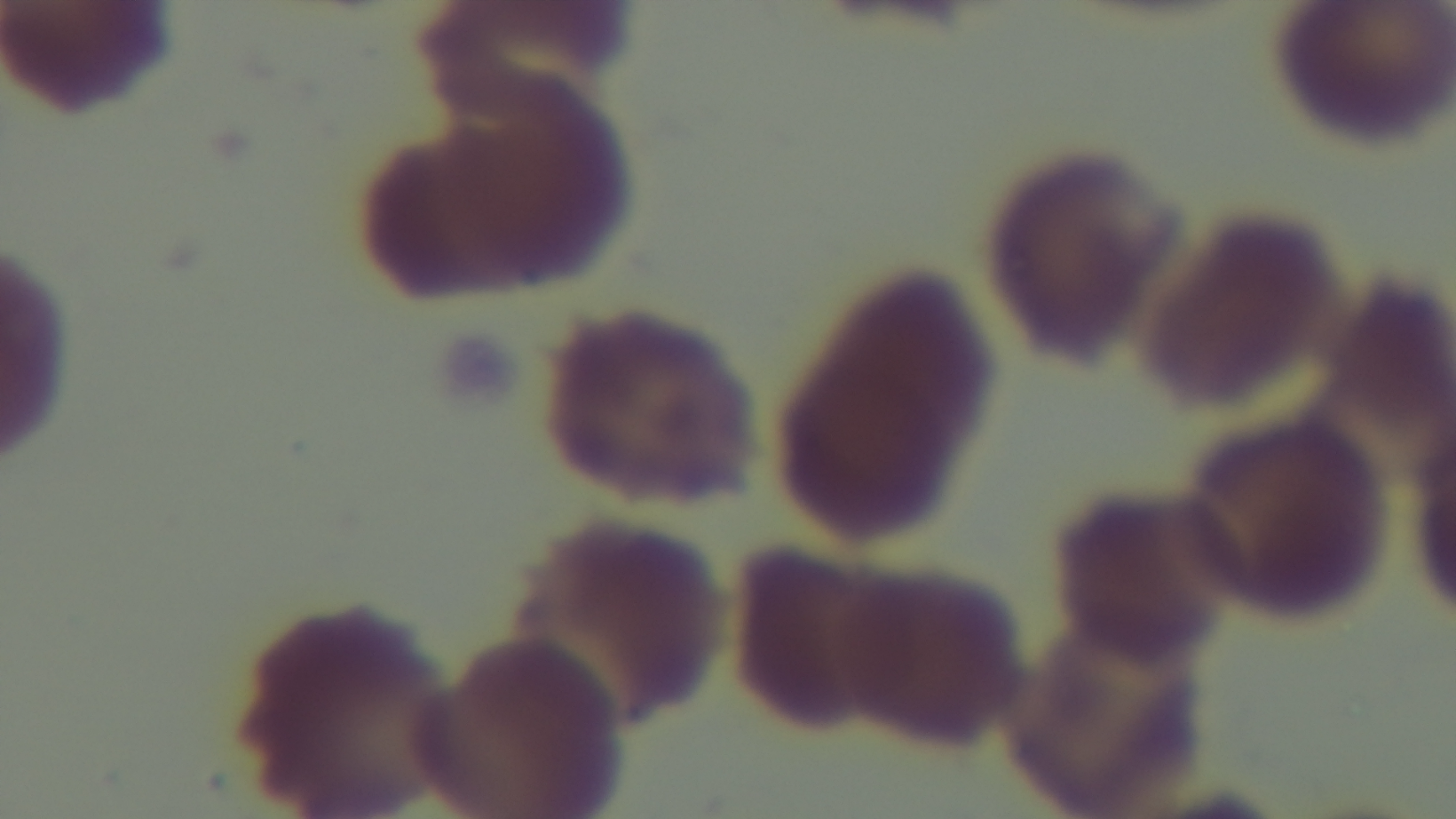
Preparation: thin. Captured with a mounted 4K digital camera. Malaria status: uninfected. Giemsa-stained. Light microscopy. One field from the slide. 100x oil-immersion objective.